Identify the blood parasite species.
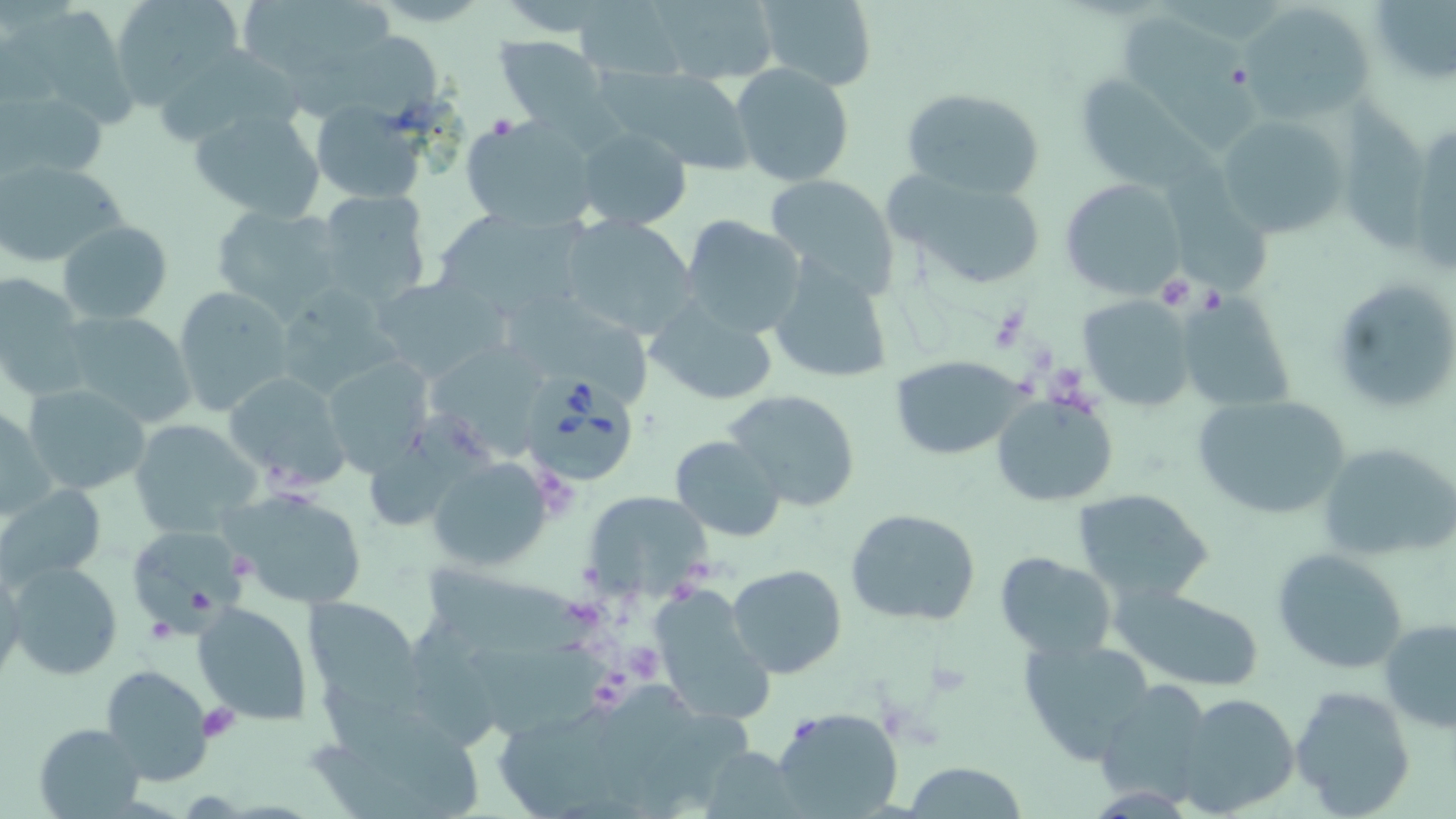

Babesia divergens.

Approximate bounding boxes as (x1,y1)-(x2,y2) corner pairs in pixels. Babesia divergens-infected red blood cell locations: (522,368)-(636,487). Platelet locations: (489,114)-(518,138), (1152,274)-(1206,310), (987,304)-(1033,354), (626,639)-(663,681), (925,661)-(971,698), (199,704)-(240,741). Uninfected red blood cell locations: (109,0)-(245,107), (239,0)-(395,71), (648,0)-(781,85), (753,0)-(878,89), (573,2)-(689,82), (1236,2)-(1375,124), (1369,3)-(1456,84), (32,5)-(133,128), (1119,13)-(1258,153), (495,35)-(607,130), (154,44)-(304,148), (730,63)-(854,187), (609,69)-(756,172), (1068,69)-(1213,188), (2,87)-(107,182), (900,87)-(1045,201), (1342,93)-(1433,253), (309,100)-(430,205), (187,107)-(328,224), (1212,110)-(1351,239), (463,116)-(598,232), (1407,120)-(1456,279), (573,126)-(692,231), (1166,151)-(1276,296), (0,159)-(129,270), (884,166)-(1049,291), (763,174)-(900,295), (1061,178)-(1183,299), (313,189)-(434,308), (211,205)-(346,319), (429,206)-(587,321), (557,213)-(698,340), (681,216)-(806,337), (59,219)-(172,325), (766,261)-(893,384), (0,271)-(93,401), (369,275)-(508,385), (1329,277)-(1456,416), (270,285)-(404,404), (173,287)-(294,415), (1187,290)-(1298,407), (1080,294)-(1197,410), (644,299)-(778,407), (521,302)-(657,400), (58,309)-(197,430), (438,344)-(549,460), (320,354)-(434,476), (888,356)-(1030,459), (224,371)-(352,492), (22,383)-(152,496), (723,389)-(862,512), (991,393)-(1118,507), (1193,394)-(1353,520), (0,405)-(58,524), (371,411)-(493,526), (129,419)-(262,539), (670,435)-(784,539), (1315,439)-(1456,564), (427,457)-(554,570), (2,483)-(106,587), (222,485)-(369,610), (1072,488)-(1215,603), (584,490)-(711,600), (844,506)-(983,625), (125,521)-(254,636), (1270,549)-(1409,674), (994,552)-(1117,660), (5,560)-(123,680), (0,562)-(25,686), (421,563)-(612,654), (727,564)-(848,680), (647,582)-(775,727), (1113,587)-(1265,692), (305,596)-(426,709), (193,600)-(314,726), (1380,619)-(1455,735), (1015,635)-(1160,767), (465,636)-(611,731), (100,666)-(213,785), (1095,682)-(1214,805), (609,684)-(689,796), (1291,686)-(1416,815), (1171,692)-(1300,816), (311,703)-(490,819), (771,706)-(904,819), (495,721)-(610,817), (35,722)-(146,817), (900,762)-(1029,819). Thin blood smear. Single field of view. Captured at 1000x magnification. May-Grünwald-Giemsa-stained preparation. Light microscopy. Image is 1456×819 pixels.